Outline each blood parasite and name the species.
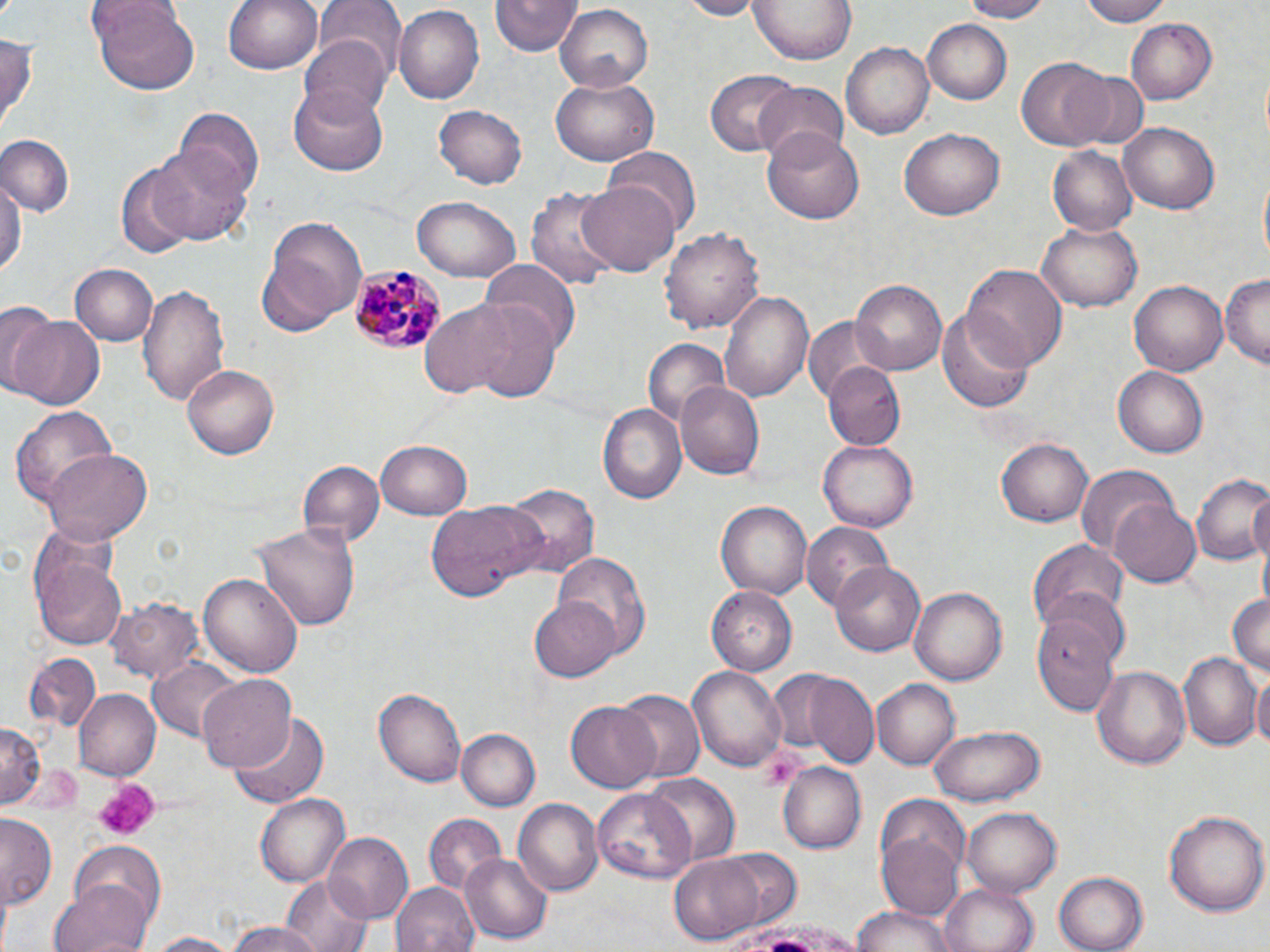

Approximate bounding boxes as (x1, y1, x2, y2) in pixels.
Plasmodium malariae-infected red blood cells: (347, 264, 448, 356).
No Plasmodium falciparum, Plasmodium ovale, Plasmodium vivax, Babesia divergens, or Trypanosoma brucei observed.

Uninfected red blood cell locations: (88, 0, 199, 94), (225, 0, 324, 75), (672, 0, 767, 19), (752, 0, 855, 65), (957, 0, 1056, 23), (1077, 0, 1173, 26), (312, 1, 405, 79), (489, 2, 579, 57), (393, 5, 484, 104), (553, 5, 655, 90), (923, 20, 1012, 104), (1125, 20, 1220, 106), (0, 30, 38, 130), (299, 35, 391, 124), (840, 41, 935, 140), (1018, 58, 1112, 149), (706, 71, 796, 156), (1070, 71, 1147, 149), (551, 77, 660, 165), (753, 83, 848, 165), (290, 86, 388, 175), (431, 104, 528, 190), (176, 106, 262, 199), (1119, 122, 1219, 213), (899, 127, 1006, 220), (763, 128, 863, 223), (0, 134, 75, 216), (152, 145, 253, 245), (607, 145, 700, 237), (1048, 145, 1139, 237), (115, 164, 195, 257), (0, 177, 24, 284), (578, 178, 679, 276), (527, 187, 620, 291), (412, 194, 520, 282), (258, 215, 368, 335), (1036, 223, 1141, 312), (662, 225, 764, 338), (479, 261, 581, 356), (964, 263, 1067, 368), (71, 265, 157, 345), (1222, 274, 1270, 366), (1130, 279, 1228, 377), (850, 280, 945, 376), (136, 283, 231, 405), (720, 290, 814, 405), (419, 300, 521, 399), (0, 301, 58, 394), (938, 303, 1035, 413), (470, 305, 562, 402), (6, 313, 106, 413), (805, 316, 881, 401), (644, 337, 732, 433), (182, 363, 278, 459), (824, 364, 906, 448), (1113, 367, 1209, 458), (675, 378, 766, 479), (597, 401, 689, 507), (8, 402, 118, 510), (998, 435, 1094, 526), (817, 439, 916, 533), (375, 440, 471, 521), (43, 448, 152, 543), (296, 460, 384, 549), (1075, 462, 1177, 558), (1191, 472, 1270, 567), (499, 483, 599, 582), (1108, 498, 1200, 587), (423, 499, 547, 602), (716, 499, 815, 600), (731, 511, 888, 600), (253, 518, 359, 630), (801, 523, 893, 610), (31, 532, 128, 652), (1028, 537, 1129, 631), (548, 551, 650, 661), (832, 562, 925, 656), (197, 570, 304, 677), (909, 585, 1008, 684), (707, 587, 797, 675), (1042, 589, 1131, 672), (1226, 589, 1269, 677), (529, 594, 622, 682), (109, 596, 206, 683), (1032, 615, 1118, 712), (1179, 653, 1260, 750), (23, 654, 101, 733), (149, 660, 248, 743), (688, 662, 788, 770), (1092, 666, 1191, 769), (1252, 673, 1270, 755), (805, 674, 877, 766), (197, 675, 296, 775), (870, 678, 959, 770), (374, 686, 466, 788), (613, 688, 705, 784), (74, 689, 160, 782), (566, 700, 661, 792), (229, 711, 330, 810), (0, 722, 44, 808), (932, 725, 1044, 806), (457, 728, 541, 811), (779, 763, 867, 852), (643, 772, 739, 867), (595, 789, 696, 886), (255, 795, 349, 885), (515, 798, 602, 896), (961, 806, 1062, 898), (1165, 807, 1268, 917), (424, 813, 506, 891), (0, 815, 58, 909), (323, 833, 413, 925), (878, 834, 964, 922), (67, 840, 169, 935), (707, 846, 803, 931), (461, 851, 554, 944), (670, 853, 766, 943), (1055, 870, 1148, 952), (278, 876, 376, 952), (51, 877, 153, 952), (392, 880, 481, 952), (939, 884, 1039, 952), (851, 903, 956, 952), (223, 922, 329, 952), (142, 931, 245, 951). Platelet locations: (91, 780, 158, 842). Slide-level diagnosis: Plasmodium malariae. Captured at 1000x magnification. Image is 1270×952 pixels. Light microscopy. May-Grünwald-Giemsa stain. One field of a larger specimen. Thin blood smear.